Classify this cell by malaria status.
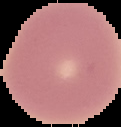

Uninfected.

Summary:
  - Preparation: thin blood smear
  - Image type: cell region segmented out of the field of view; surrounding area masked to black
  - Image size: 121×127 pixels